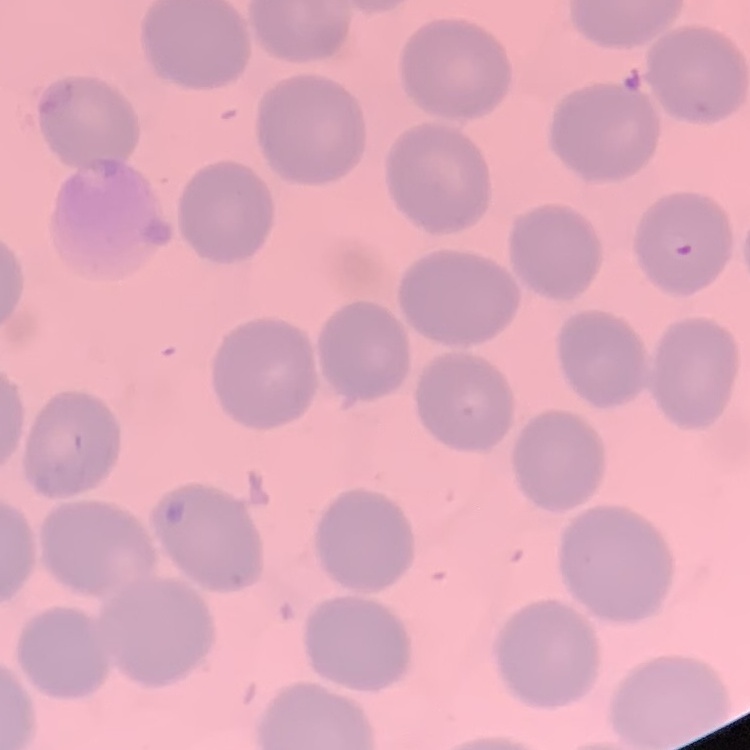

red blood cell morphology = no rouleaux formation
image type = one tile cut from a larger photomicrograph
preparation = thin blood smear
stain = Field's or Giemsa